Identify the blood parasite species.
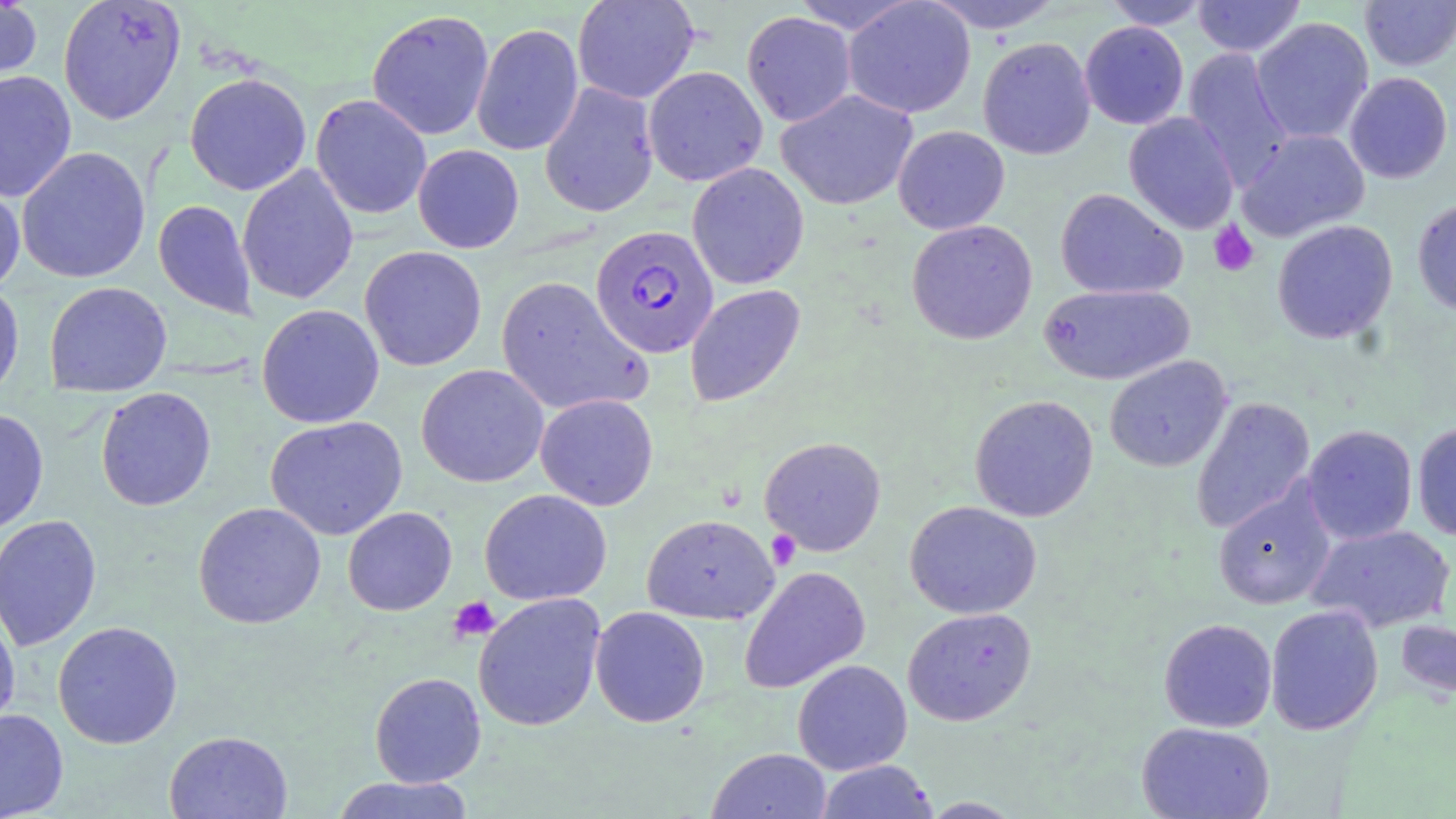
Plasmodium falciparum.

preparation = thin blood smear
modality = light microscopy
image size = 1456×819 pixels
stain = May-Grünwald-Giemsa
uninfected red blood cell locations = approximate bounding boxes as named x1/y1/x2/y2 corners in pixels: (x1=0, y1=0, x2=42, y2=92), (x1=57, y1=0, x2=186, y2=125), (x1=573, y1=0, x2=699, y2=104), (x1=788, y1=0, x2=920, y2=34), (x1=843, y1=0, x2=976, y2=119), (x1=923, y1=0, x2=1064, y2=34), (x1=1193, y1=0, x2=1306, y2=57), (x1=1359, y1=0, x2=1456, y2=71), (x1=1102, y1=1, x2=1210, y2=30), (x1=366, y1=9, x2=495, y2=141), (x1=741, y1=11, x2=856, y2=127), (x1=1251, y1=17, x2=1374, y2=144), (x1=1080, y1=21, x2=1189, y2=130), (x1=471, y1=22, x2=584, y2=156), (x1=978, y1=37, x2=1095, y2=160), (x1=1182, y1=47, x2=1293, y2=188), (x1=643, y1=66, x2=768, y2=187), (x1=0, y1=70, x2=77, y2=202), (x1=184, y1=72, x2=312, y2=196), (x1=1344, y1=72, x2=1453, y2=184), (x1=539, y1=81, x2=659, y2=218), (x1=776, y1=89, x2=918, y2=211), (x1=310, y1=94, x2=432, y2=219), (x1=1124, y1=112, x2=1240, y2=234), (x1=893, y1=125, x2=1010, y2=234), (x1=1237, y1=129, x2=1370, y2=242), (x1=413, y1=144, x2=524, y2=253), (x1=16, y1=146, x2=152, y2=284), (x1=687, y1=162, x2=809, y2=289), (x1=237, y1=164, x2=359, y2=305), (x1=0, y1=176, x2=25, y2=294), (x1=1055, y1=188, x2=1187, y2=299), (x1=1412, y1=198, x2=1456, y2=315), (x1=153, y1=199, x2=258, y2=320), (x1=906, y1=219, x2=1038, y2=345), (x1=1272, y1=220, x2=1398, y2=345), (x1=359, y1=245, x2=487, y2=371), (x1=495, y1=275, x2=652, y2=417), (x1=0, y1=279, x2=25, y2=402), (x1=44, y1=281, x2=172, y2=397), (x1=1038, y1=283, x2=1194, y2=386), (x1=685, y1=284, x2=805, y2=407), (x1=256, y1=304, x2=385, y2=428), (x1=1104, y1=356, x2=1231, y2=472), (x1=416, y1=364, x2=549, y2=488), (x1=95, y1=386, x2=216, y2=511), (x1=535, y1=393, x2=659, y2=511), (x1=969, y1=394, x2=1099, y2=522), (x1=1190, y1=397, x2=1315, y2=534), (x1=0, y1=408, x2=49, y2=534), (x1=265, y1=415, x2=408, y2=540), (x1=1412, y1=423, x2=1456, y2=540), (x1=1303, y1=424, x2=1418, y2=544), (x1=759, y1=436, x2=887, y2=557), (x1=1213, y1=483, x2=1336, y2=610), (x1=479, y1=488, x2=612, y2=606), (x1=905, y1=500, x2=1042, y2=619), (x1=192, y1=501, x2=327, y2=630), (x1=342, y1=506, x2=457, y2=616), (x1=0, y1=514, x2=103, y2=652), (x1=642, y1=514, x2=778, y2=624), (x1=1306, y1=524, x2=1453, y2=633), (x1=738, y1=566, x2=871, y2=694), (x1=473, y1=593, x2=606, y2=731), (x1=0, y1=604, x2=21, y2=733), (x1=1265, y1=604, x2=1384, y2=735), (x1=591, y1=606, x2=710, y2=727), (x1=902, y1=607, x2=1037, y2=726), (x1=1395, y1=617, x2=1455, y2=701), (x1=1159, y1=618, x2=1276, y2=732), (x1=52, y1=620, x2=183, y2=749), (x1=792, y1=659, x2=912, y2=775), (x1=369, y1=671, x2=487, y2=787), (x1=0, y1=708, x2=69, y2=818), (x1=1136, y1=721, x2=1275, y2=819), (x1=164, y1=730, x2=293, y2=819), (x1=707, y1=748, x2=833, y2=819), (x1=815, y1=760, x2=938, y2=818), (x1=329, y1=775, x2=477, y2=818), (x1=919, y1=797, x2=1024, y2=818)
field of view = one of a larger specimen
magnification = 1000x
platelet locations = approximate bounding boxes as named x1/y1/x2/y2 corners in pixels: (x1=1208, y1=220, x2=1260, y2=277), (x1=766, y1=529, x2=801, y2=570), (x1=448, y1=596, x2=500, y2=643)
Plasmodium falciparum-infected red blood cell locations = approximate bounding boxes as named x1/y1/x2/y2 corners in pixels: (x1=590, y1=225, x2=718, y2=359)